Assess this cell for malaria.
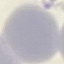
It is uninfected.

Thin blood film. Photographed with a smartphone camera at the microscope eyepiece. Automatically extracted cell patch, resized to 64 × 64 pixels. Giemsa stain.